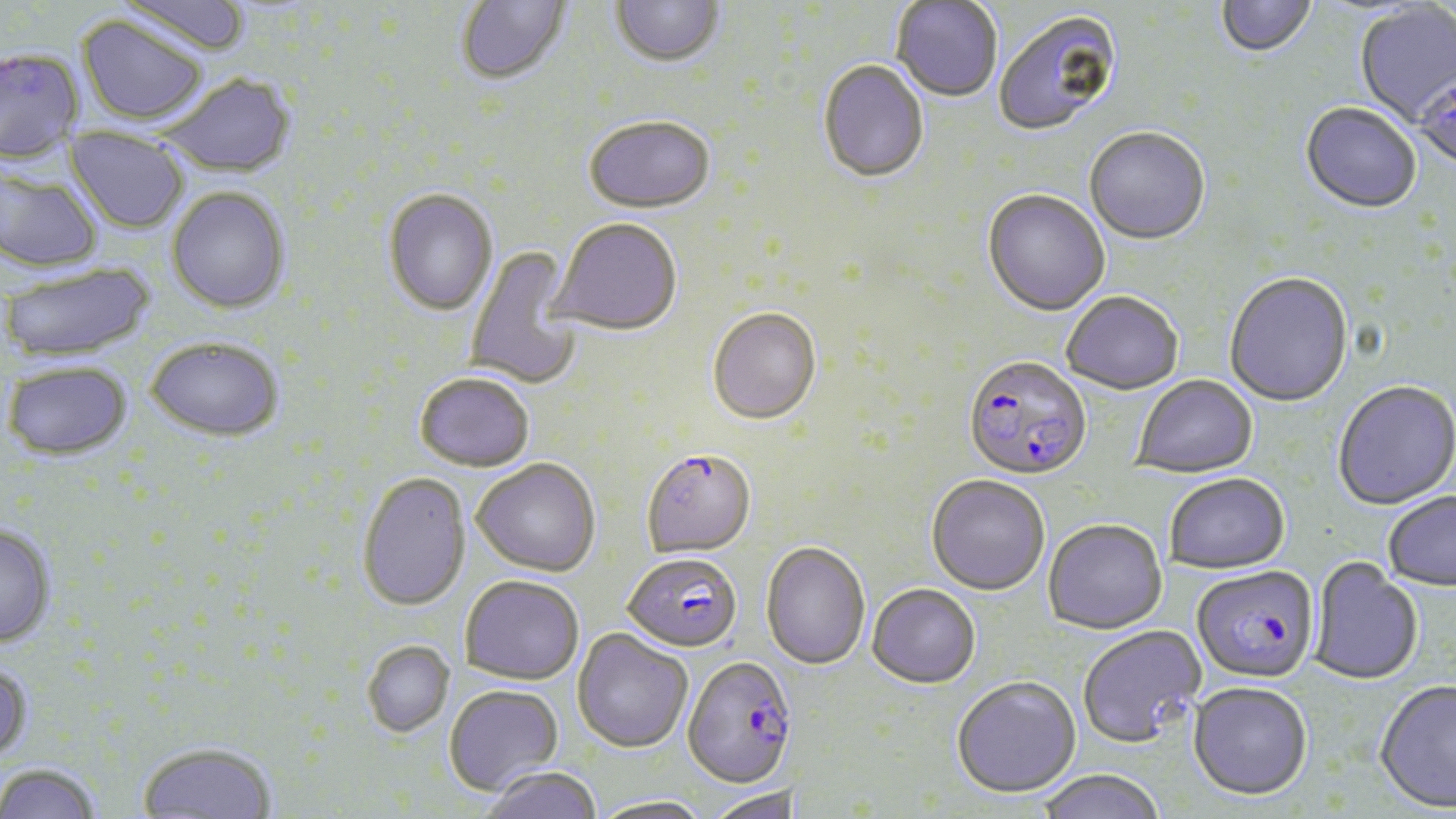

slide-level diagnosis = Plasmodium falciparum
preparation = thin blood smear
image size = 1456×819 pixels
field of view = single
modality = light microscopy
uninfected red blood cell locations = approximate bounding boxes as (x1, y1, x2, y2) in pixels: (116, 0, 252, 58), (455, 0, 573, 88), (1217, 0, 1317, 61), (610, 1, 725, 71), (891, 1, 1003, 104), (1356, 4, 1456, 125), (993, 10, 1124, 138), (77, 15, 209, 126), (817, 62, 929, 186), (1413, 71, 1456, 175), (159, 73, 298, 178), (1300, 105, 1421, 216), (583, 119, 716, 217), (65, 126, 189, 234), (1084, 129, 1210, 248), (0, 167, 102, 273), (167, 187, 290, 314), (383, 190, 498, 317), (982, 191, 1109, 318), (549, 220, 682, 339), (465, 246, 584, 390), (1, 261, 155, 363), (1223, 274, 1354, 409), (1061, 293, 1183, 397), (708, 309, 822, 427), (146, 336, 285, 442), (3, 361, 133, 460), (414, 373, 534, 472), (1133, 376, 1258, 480), (1332, 382, 1456, 511), (472, 458, 601, 576), (357, 473, 470, 612), (926, 475, 1050, 596), (1164, 475, 1290, 576), (1383, 493, 1456, 593), (1043, 520, 1167, 636), (0, 525, 56, 647), (761, 542, 870, 670), (1308, 558, 1423, 687), (460, 575, 584, 685), (866, 585, 980, 690), (1077, 625, 1206, 750), (572, 628, 693, 753), (362, 641, 455, 737), (0, 662, 32, 763), (950, 677, 1082, 800), (1374, 681, 1456, 815), (444, 684, 563, 796), (1188, 684, 1312, 804), (138, 742, 276, 819), (0, 763, 102, 819), (483, 766, 602, 819), (1033, 770, 1167, 819), (705, 787, 799, 819), (588, 796, 714, 819)
Plasmodium falciparum-infected red blood cell locations = approximate bounding boxes as (x1, y1, x2, y2) in pixels: (0, 47, 83, 162), (963, 358, 1091, 483), (641, 449, 756, 558), (623, 551, 741, 652), (1191, 568, 1319, 685), (682, 656, 796, 789)
magnification = 1000x
stain = May-Grünwald-Giemsa